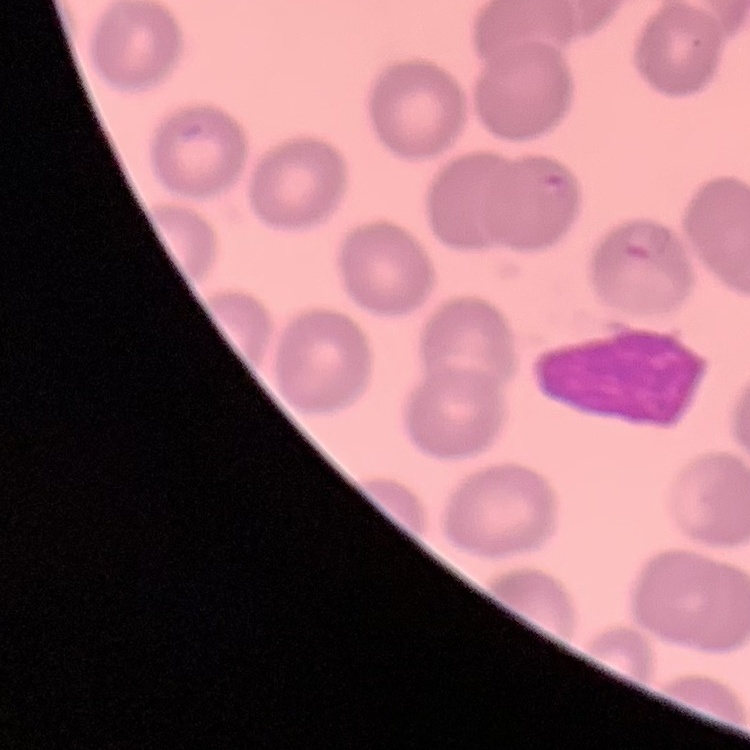
red blood cell morphology = no rouleaux formation
preparation = thin blood smear
image type = one tile cut from a larger photomicrograph
stain = Field's or Giemsa